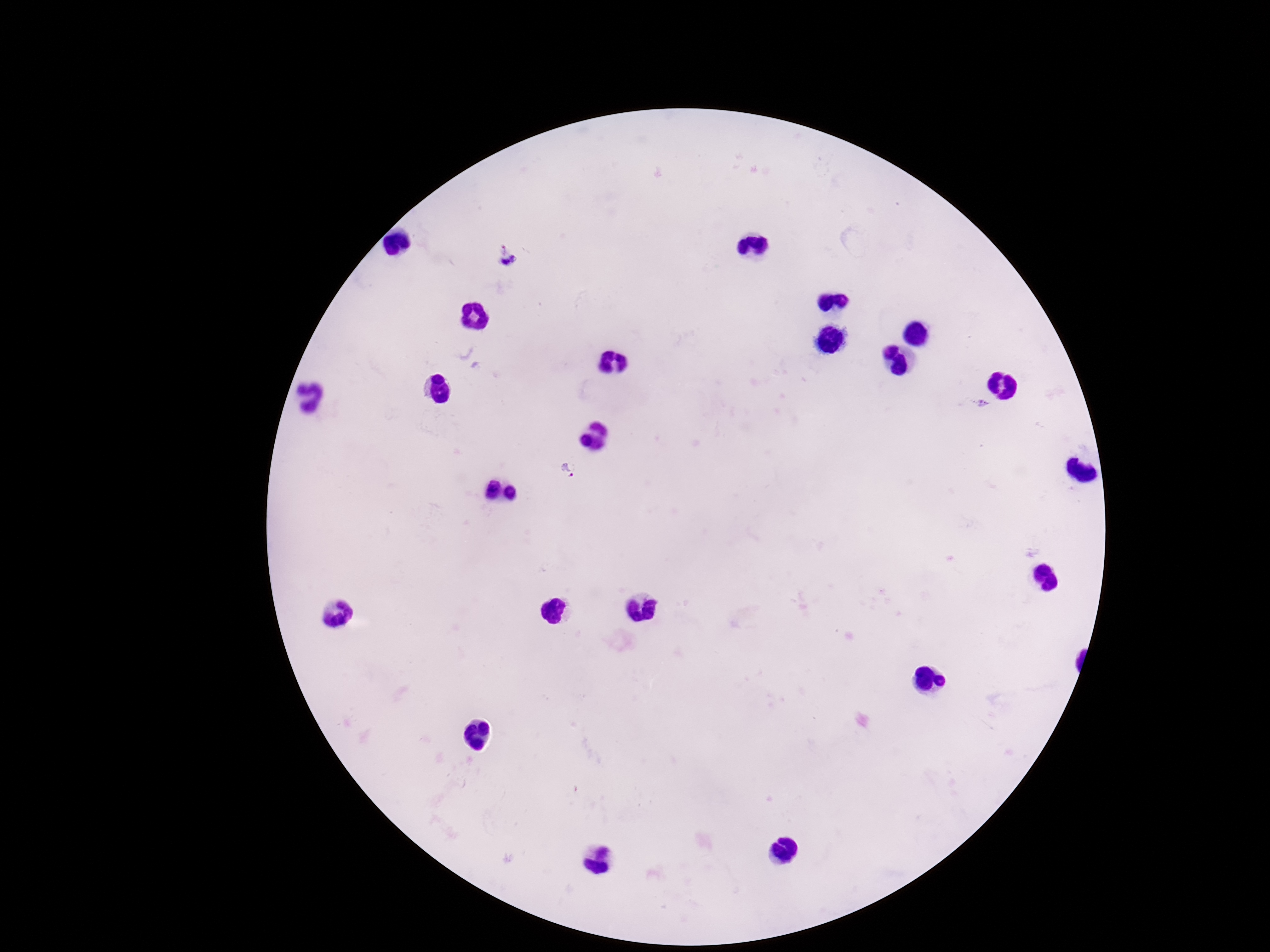
Approximate centers as {x, y} in pixels. Plasmodium parasite locations: {507, 256}, {980, 403}, {569, 472}. Giemsa-stained preparation. Thick blood film. Smartphone photograph taken through the microscope eyepiece. Image is 1270×952 pixels. 100x magnification. Patient malaria status: infected. Single field of view.